Identify the parasite.
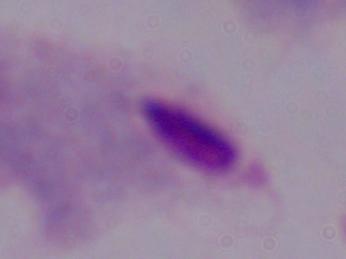

A trichomonad.

Photomicrograph. Captured at 1000x magnification.